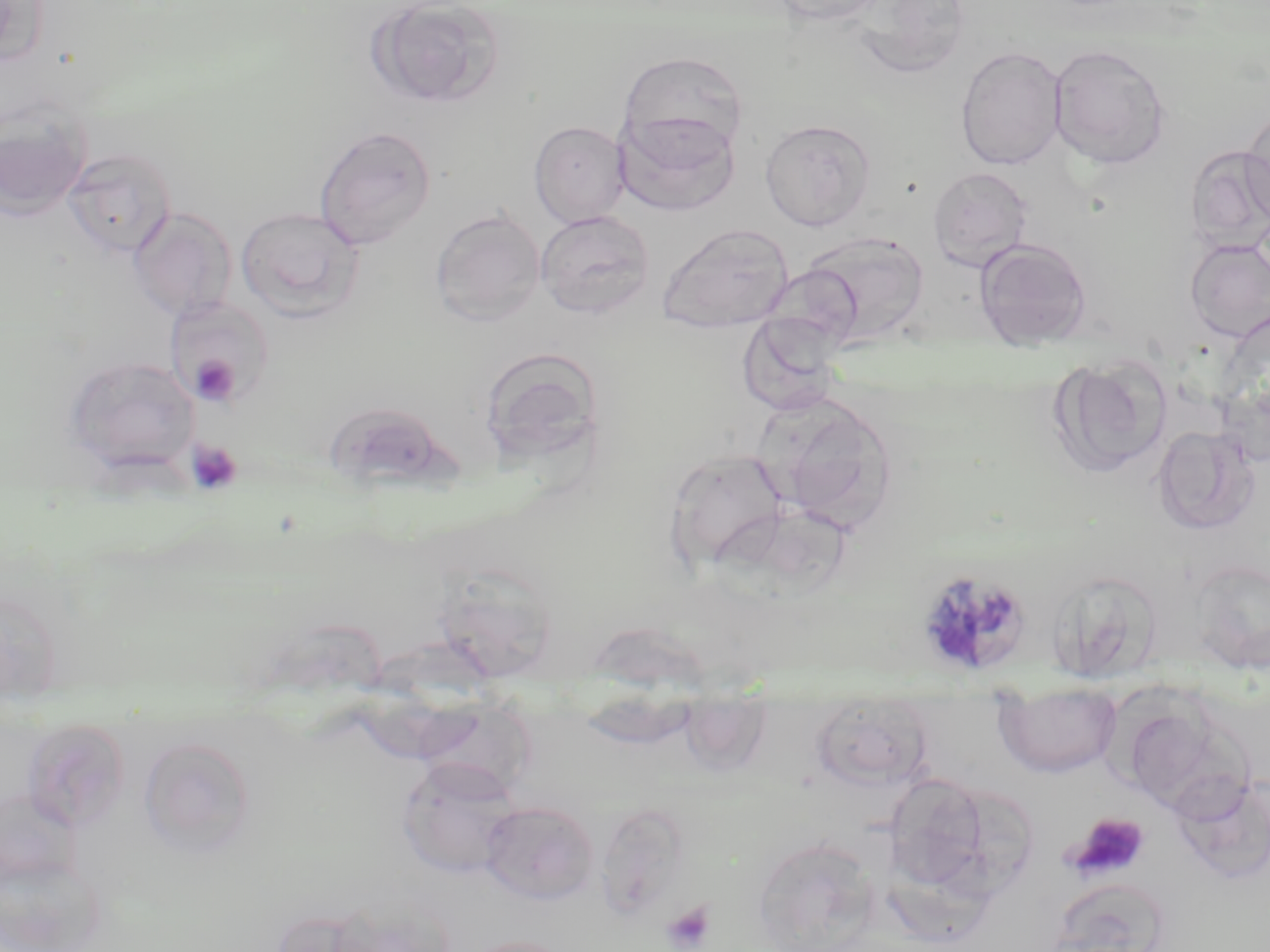
slide_level_diagnosis: Plasmodium malariae
uninfected_red_blood_cell_locations: 'approximate bounding boxes as named x1/y1/x2/y2 corners in pixels: (x1=0, y1=0, x2=49, y2=67), (x1=366, y1=0, x2=506, y2=109), (x1=769, y1=0, x2=893, y2=26), (x1=847, y1=1, x2=971, y2=79), (x1=1048, y1=44, x2=1172, y2=169), (x1=955, y1=45, x2=1067, y2=170), (x1=627, y1=58, x2=749, y2=170), (x1=0, y1=97, x2=92, y2=222), (x1=1242, y1=106, x2=1270, y2=228), (x1=614, y1=110, x2=740, y2=216), (x1=760, y1=118, x2=876, y2=231), (x1=529, y1=121, x2=630, y2=227), (x1=314, y1=125, x2=437, y2=249), (x1=1185, y1=144, x2=1270, y2=253), (x1=62, y1=146, x2=177, y2=258), (x1=928, y1=166, x2=1033, y2=271), (x1=236, y1=206, x2=365, y2=322), (x1=128, y1=207, x2=238, y2=322), (x1=430, y1=208, x2=546, y2=327), (x1=535, y1=210, x2=654, y2=319), (x1=657, y1=223, x2=794, y2=333), (x1=799, y1=232, x2=929, y2=346), (x1=974, y1=238, x2=1092, y2=348), (x1=1184, y1=238, x2=1270, y2=343), (x1=167, y1=298, x2=273, y2=406), (x1=741, y1=318, x2=841, y2=418), (x1=487, y1=350, x2=600, y2=465), (x1=1049, y1=354, x2=1172, y2=478), (x1=63, y1=355, x2=200, y2=474), (x1=1217, y1=375, x2=1269, y2=468), (x1=762, y1=395, x2=899, y2=533), (x1=325, y1=402, x2=451, y2=491), (x1=1152, y1=425, x2=1261, y2=535), (x1=665, y1=448, x2=790, y2=572), (x1=1189, y1=558, x2=1270, y2=674), (x1=430, y1=563, x2=560, y2=679), (x1=1045, y1=569, x2=1162, y2=685), (x1=585, y1=621, x2=709, y2=693), (x1=366, y1=640, x2=504, y2=759), (x1=993, y1=681, x2=1122, y2=778), (x1=677, y1=694, x2=773, y2=777), (x1=1116, y1=696, x2=1242, y2=814), (x1=809, y1=702, x2=935, y2=791), (x1=20, y1=721, x2=129, y2=833), (x1=138, y1=734, x2=257, y2=858), (x1=396, y1=757, x2=522, y2=878), (x1=1169, y1=770, x2=1270, y2=886), (x1=884, y1=772, x2=991, y2=891), (x1=950, y1=788, x2=1037, y2=897), (x1=480, y1=801, x2=599, y2=905), (x1=601, y1=806, x2=689, y2=918), (x1=750, y1=837, x2=882, y2=952), (x1=1046, y1=877, x2=1174, y2=952), (x1=268, y1=907, x2=387, y2=952), (x1=463, y1=935, x2=574, y2=952)'
magnification: 1000x
image_size: 1270×952 pixels
preparation: thin blood smear
modality: optical microscopy
field_of_view: one of a larger specimen
stain: May-Grünwald-Giemsa
platelet_locations: 'approximate bounding boxes as named x1/y1/x2/y2 corners in pixels: (x1=190, y1=355, x2=239, y2=405), (x1=185, y1=441, x2=243, y2=496), (x1=1065, y1=812, x2=1150, y2=881), (x1=662, y1=900, x2=717, y2=952)'
plasmodium_malariae_infected_red_blood_cell_locations: 'approximate bounding boxes as named x1/y1/x2/y2 corners in pixels: (x1=922, y1=568, x2=1030, y2=673)'